Assess this cell for malaria.
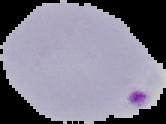

Parasitized.

Segmented cell region on a black background. Image is 166×124 pixels. From a thin blood smear.